Locate every malaria parasite.
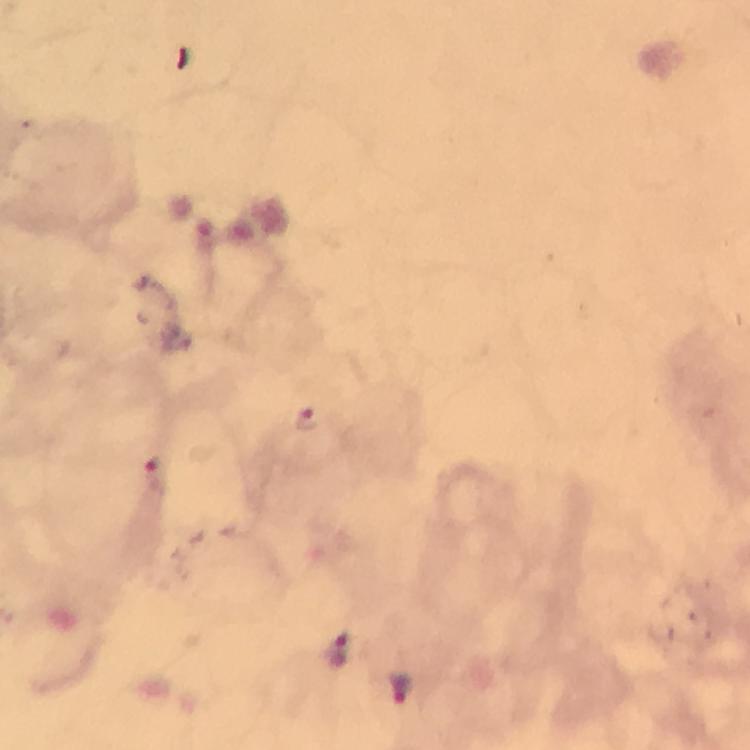
Approximate centers as [x, y] in pixels.
Malaria parasites: [305, 417], [154, 472], [337, 650], [401, 686].

Photographed through the microscope with a smartphone camera. A crop from one field of view. Giemsa-stained preparation. Image is 750×750 pixels. Thick smear. Immersion oil was used. From a malaria diagnostic workup. 100x magnification.